Give the preparation type.
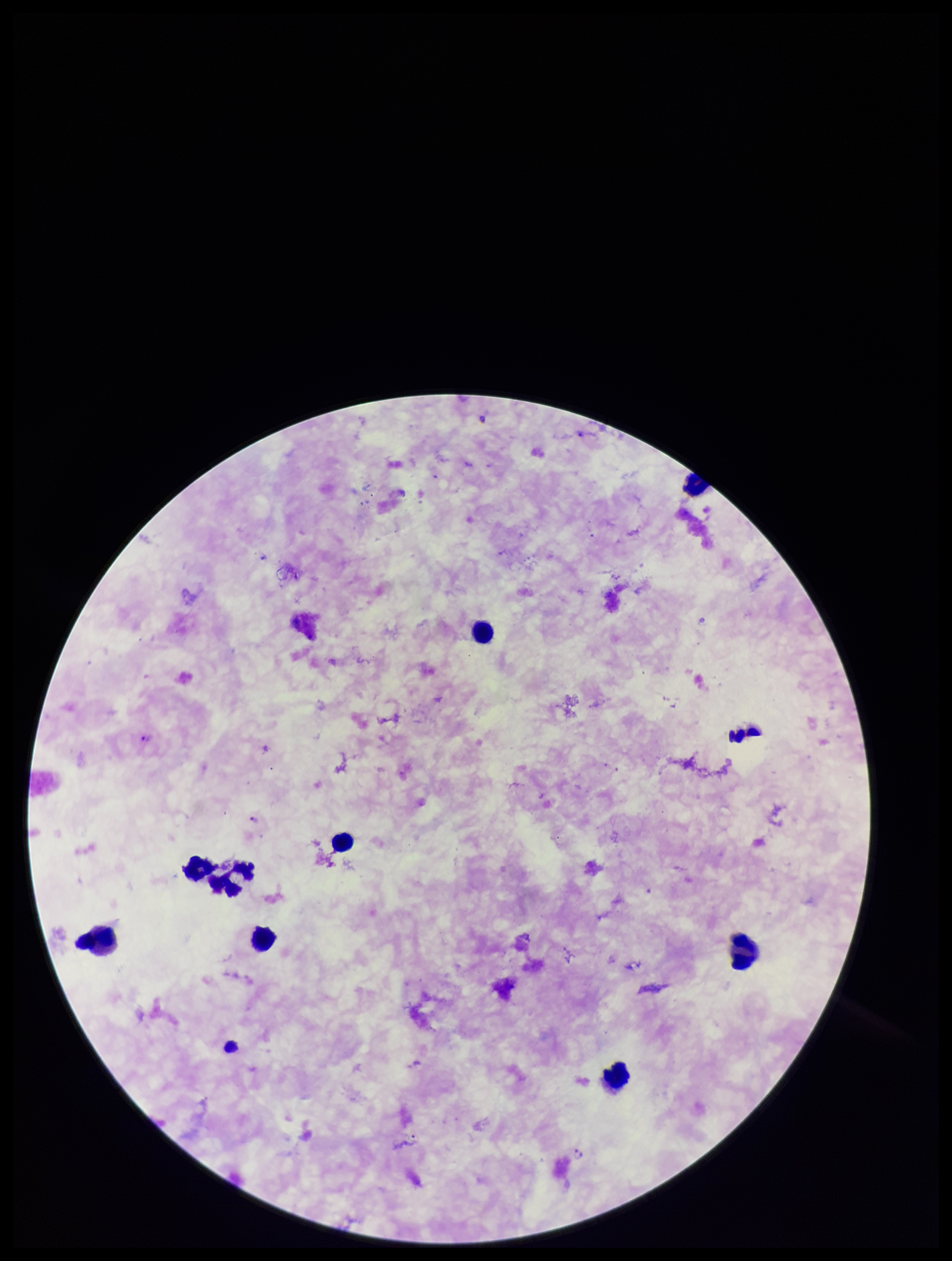

It is a thick blood smear.

Giemsa stain. Single field of view. Image is 952×1261 pixels. Plasmodium parasites: detected. Patient malaria status: infected. Leukocyte count: 9. Parasite count: 3. Species reported for this patient: Plasmodium falciparum. Smartphone photograph taken through the eyepiece of a microscope.